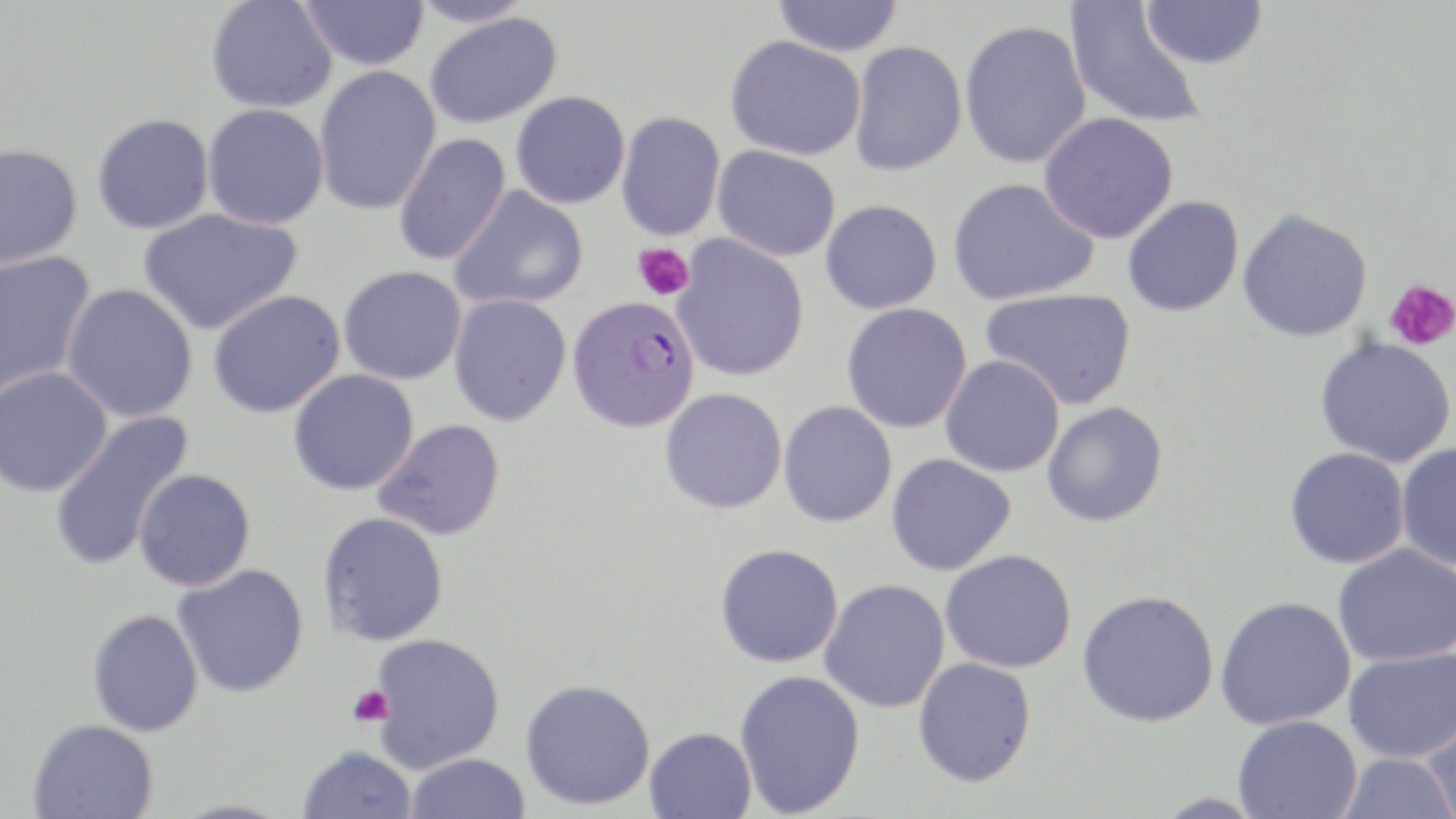

{
  "slide_level_diagnosis": "Plasmodium falciparum",
  "magnification": "1000x",
  "stain": "May-Grünwald-Giemsa",
  "field_of_view": "one of a larger specimen",
  "modality": "light microscopy",
  "preparation": "thin blood film",
  "plasmodium_falciparum_infected_red_blood_cell_locations": "approximate bounding boxes as (x1,y1)-(x2,y2) corner pairs in pixels: (566,295)-(700,433)",
  "image_size": "1456×819 pixels",
  "uninfected_red_blood_cell_locations": "approximate bounding boxes as (x1,y1)-(x2,y2) corner pairs in pixels: (206,0)-(337,114), (300,0)-(429,71), (409,0)-(534,28), (772,0)-(903,57), (1141,0)-(1267,70), (1064,1)-(1206,131), (424,12)-(562,128), (958,19)-(1092,169), (725,35)-(866,161), (849,40)-(968,176), (313,65)-(441,217), (511,91)-(630,209), (203,103)-(329,230), (616,112)-(725,241), (1039,112)-(1179,244), (92,113)-(214,235), (393,133)-(511,266), (0,143)-(83,270), (712,146)-(841,262), (948,177)-(1099,306), (449,185)-(588,311), (1122,196)-(1244,317), (820,200)-(942,314), (138,208)-(302,335), (1237,208)-(1373,342), (672,235)-(809,382), (0,251)-(96,398), (338,265)-(467,385), (62,284)-(198,423), (981,289)-(1137,410), (208,290)-(346,418), (449,294)-(572,426), (841,303)-(973,434), (1315,338)-(1455,468), (940,356)-(1065,477), (0,367)-(113,497), (288,369)-(419,495), (659,388)-(788,515), (778,401)-(898,527), (1042,402)-(1168,527), (48,411)-(194,571), (374,419)-(505,541), (1396,443)-(1456,570), (1285,448)-(1410,569), (886,454)-(1017,576), (133,468)-(255,591), (317,511)-(449,647), (715,543)-(844,668), (1332,543)-(1456,667), (939,549)-(1077,673), (173,564)-(309,698), (820,579)-(950,714), (1077,590)-(1219,727), (1215,596)-(1356,731), (87,609)-(204,737), (369,632)-(504,773), (1343,647)-(1456,763), (913,657)-(1037,787), (734,669)-(866,817), (520,678)-(656,810), (1420,713)-(1456,819), (1233,715)-(1363,819), (27,719)-(158,819), (644,727)-(757,819), (297,746)-(417,819), (1336,752)-(1455,819), (405,753)-(530,818)",
  "platelet_locations": "approximate bounding boxes as (x1,y1)-(x2,y2) corner pairs in pixels: (633,242)-(694,301), (1384,278)-(1456,352), (347,685)-(393,728)"
}